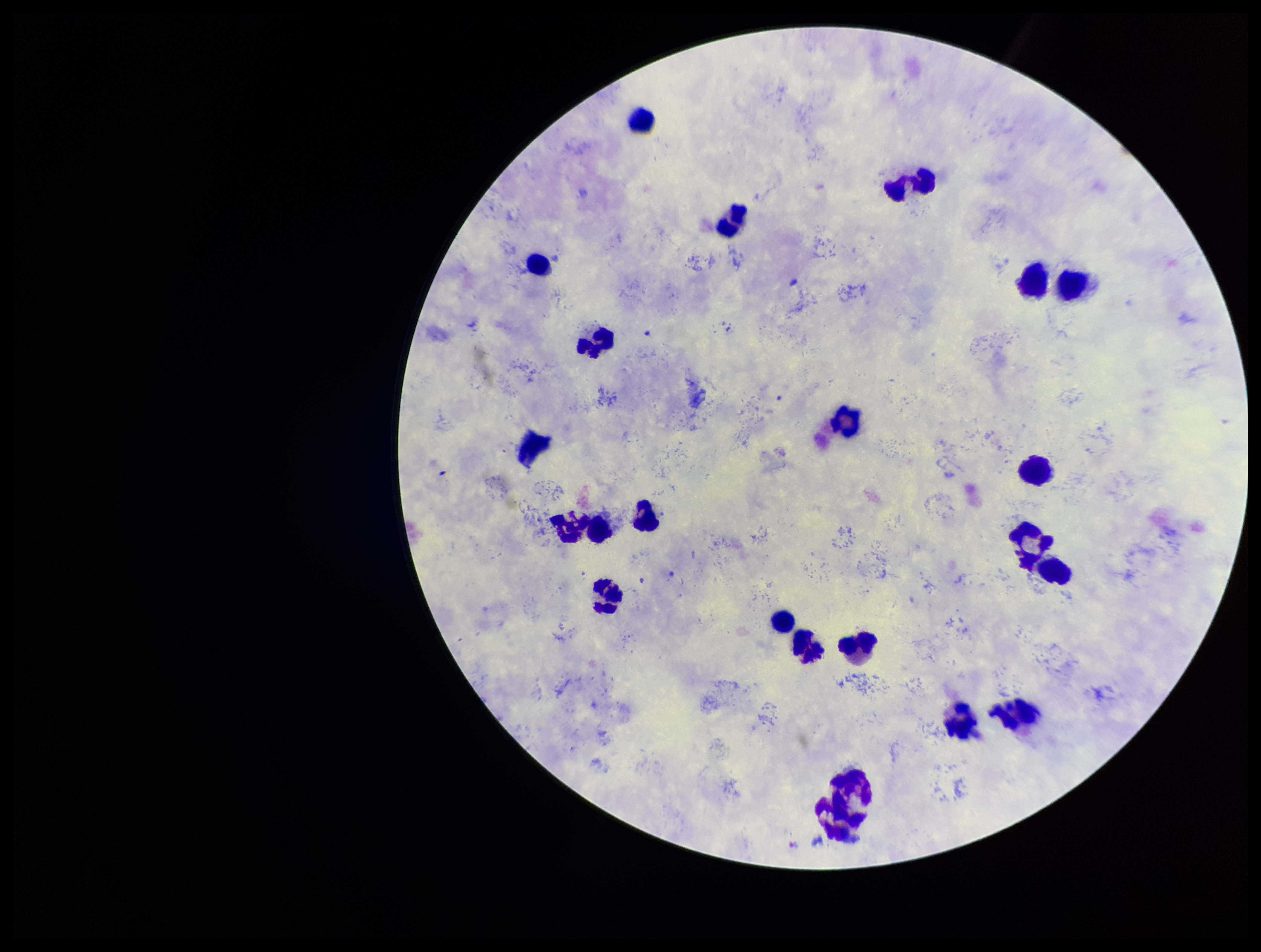
Plasmodium parasites: none detected. Stained with Giemsa. Species reported for this patient: Plasmodium vivax. Photographed through the microscope eyepiece with a smartphone camera. Leukocyte count: 23. Preparation: thick smear. Parasite count: 0. Patient malaria status: positive. Image is 1261×952 pixels. One field from this slide.